Assess this cell for malaria.
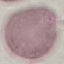

It is uninfected.

{
  "preparation": "thin smear",
  "capture": "smartphone through the microscope eyepiece",
  "stain": "Giemsa",
  "image_type": "cell patch, automatically extracted from a larger field of view and resized to 64 × 64 pixels"
}